State which parasite is depicted.
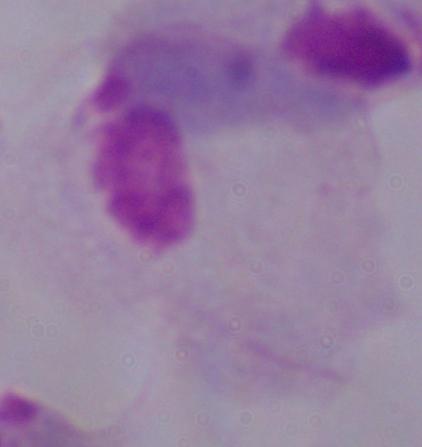

A trichomonad.

Captured at 1000x magnification. Photomicrograph.